Give the position of every Plasmodium parasite.
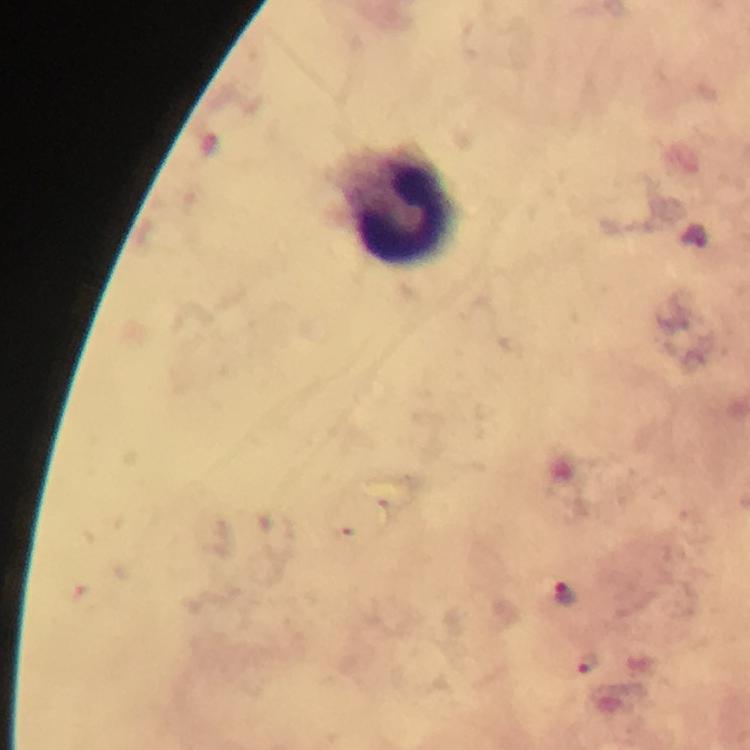

Approximate centers as [x, y] in pixels.
Plasmodium parasites: [565, 594], [589, 664].

Leukocyte locations: [405, 211]. Cropped region of a single field of view. Photographed with a smartphone mounted on the microscope. Thick blood film. Image is 750×750 pixels. Immersion oil applied. From a diagnostic examination for malaria. 100x magnification. Giemsa stain.